Comment on the morphology of the erythrocytes.
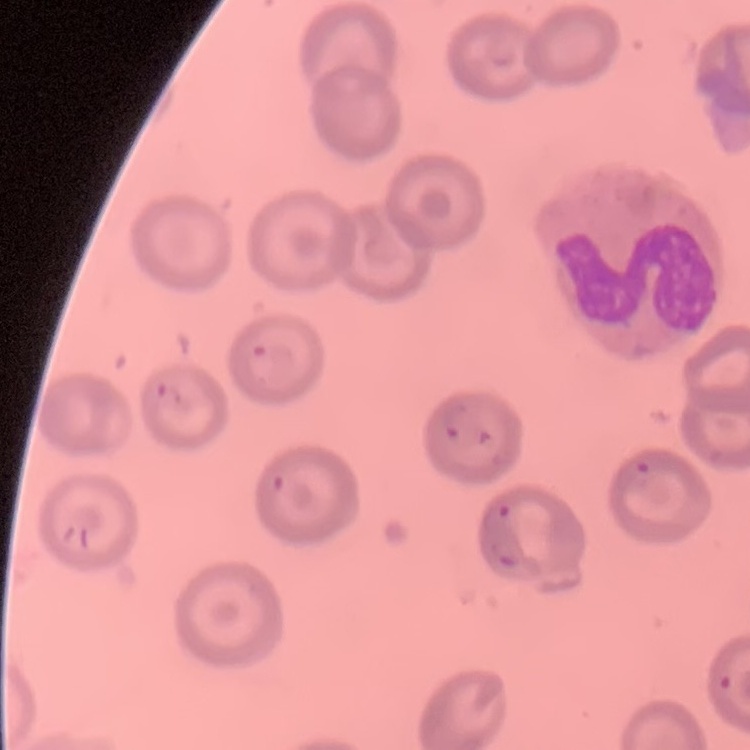
They show no rouleaux formation.

Summary:
  - Image type: one tile cut from a larger photomicrograph
  - Stain: Field's or Giemsa
  - Preparation: thin peripheral smear